Classify this cell by malaria status.
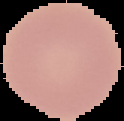
Uninfected.

{
  "image_size": "124×121 pixels",
  "image_type": "segmented cell region on a black background",
  "preparation": "thin blood smear"
}